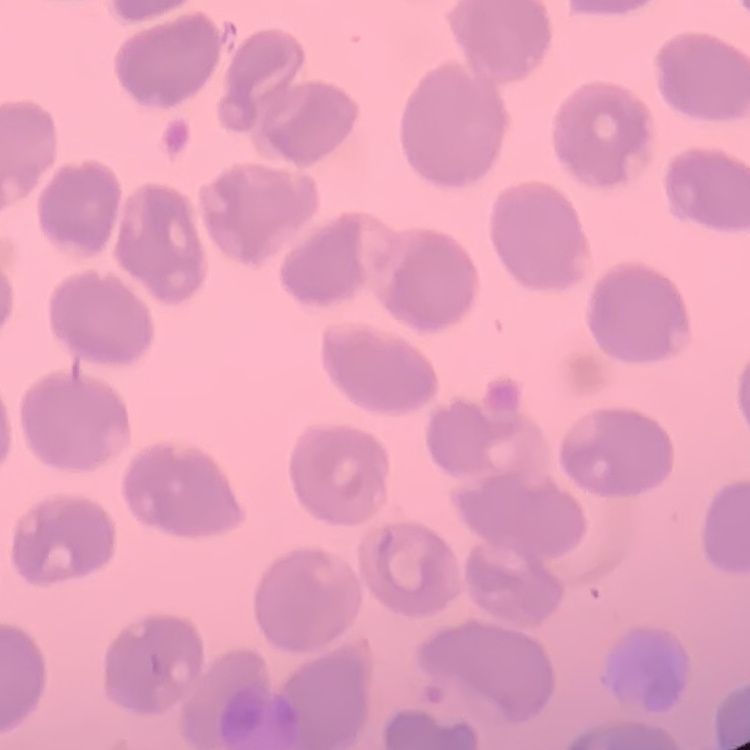

{
  "red_blood_cell_morphology": "no rouleaux formation",
  "preparation": "thin blood smear",
  "image_type": "square crop of a larger photomicrograph",
  "stain": "Field's or Giemsa"
}